Locate every Plasmodium parasite.
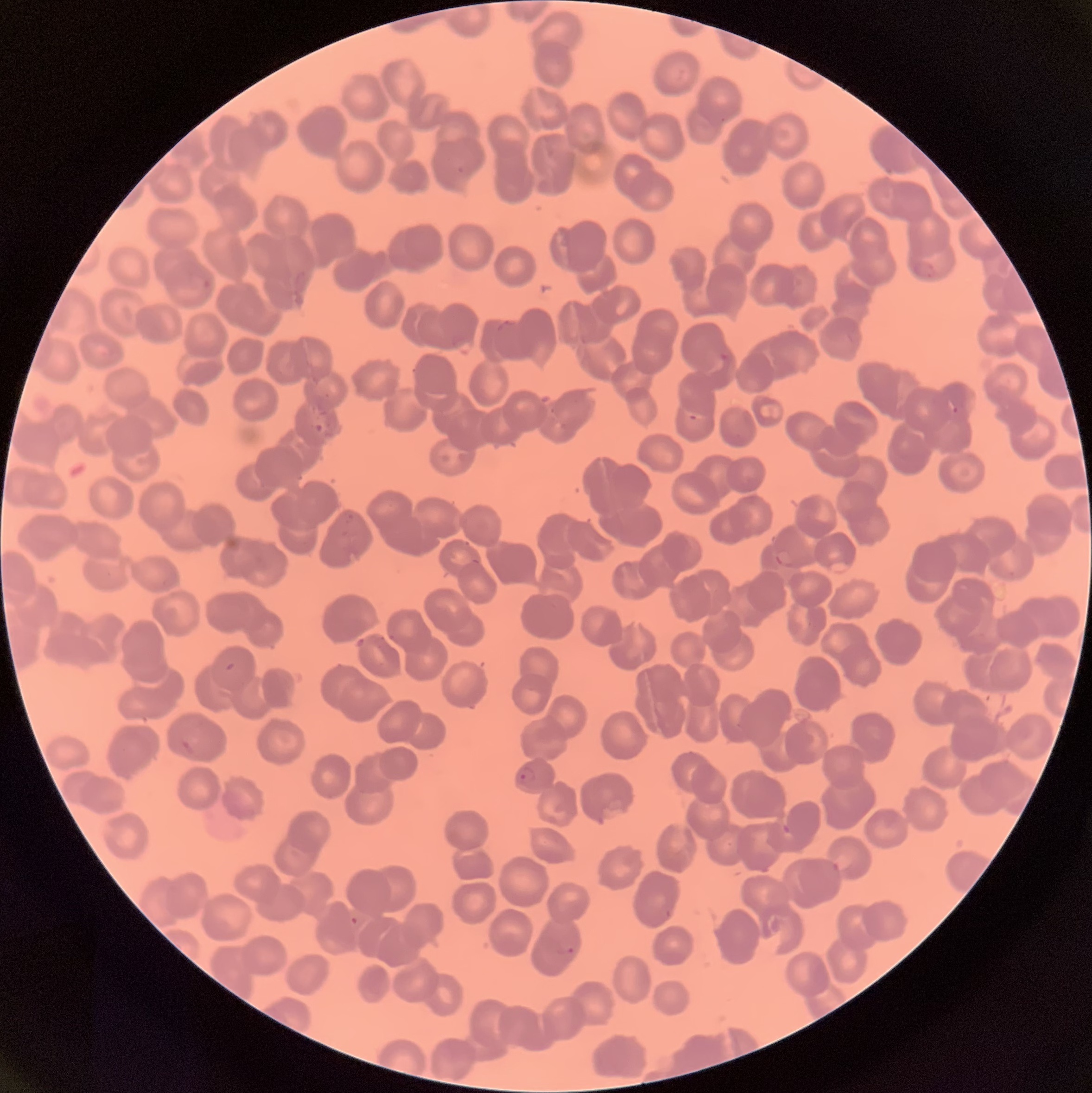

Approximate bounding boxes as (x1, y1, x2, y2) in pixels.
Plasmodium parasites: (455, 165, 468, 176), (912, 261, 940, 279), (202, 278, 212, 290), (496, 318, 519, 331), (718, 352, 730, 362), (946, 399, 958, 415), (688, 413, 698, 421), (313, 421, 324, 434), (776, 550, 794, 570), (225, 661, 236, 672), (179, 738, 197, 756), (516, 766, 536, 786), (780, 823, 791, 834), (663, 909, 673, 919), (350, 915, 359, 925), (557, 946, 576, 956).

Light microscopy. Image is 1092×1093 pixels. Thin blood smear. The red blood cells show rouleaux formation.